Assess this cell for malaria.
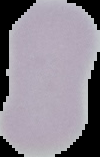

It is uninfected.

From a thin blood film. Segmented cell region on a black background. Image is 100×157 pixels.